State which parasite is depicted.
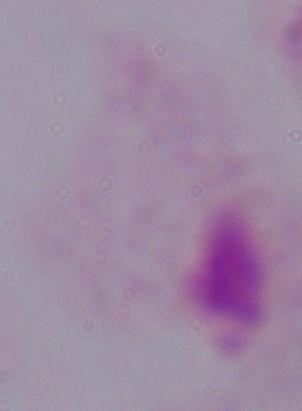
A trichomonad.

Photomicrograph. Captured at 1000x magnification.